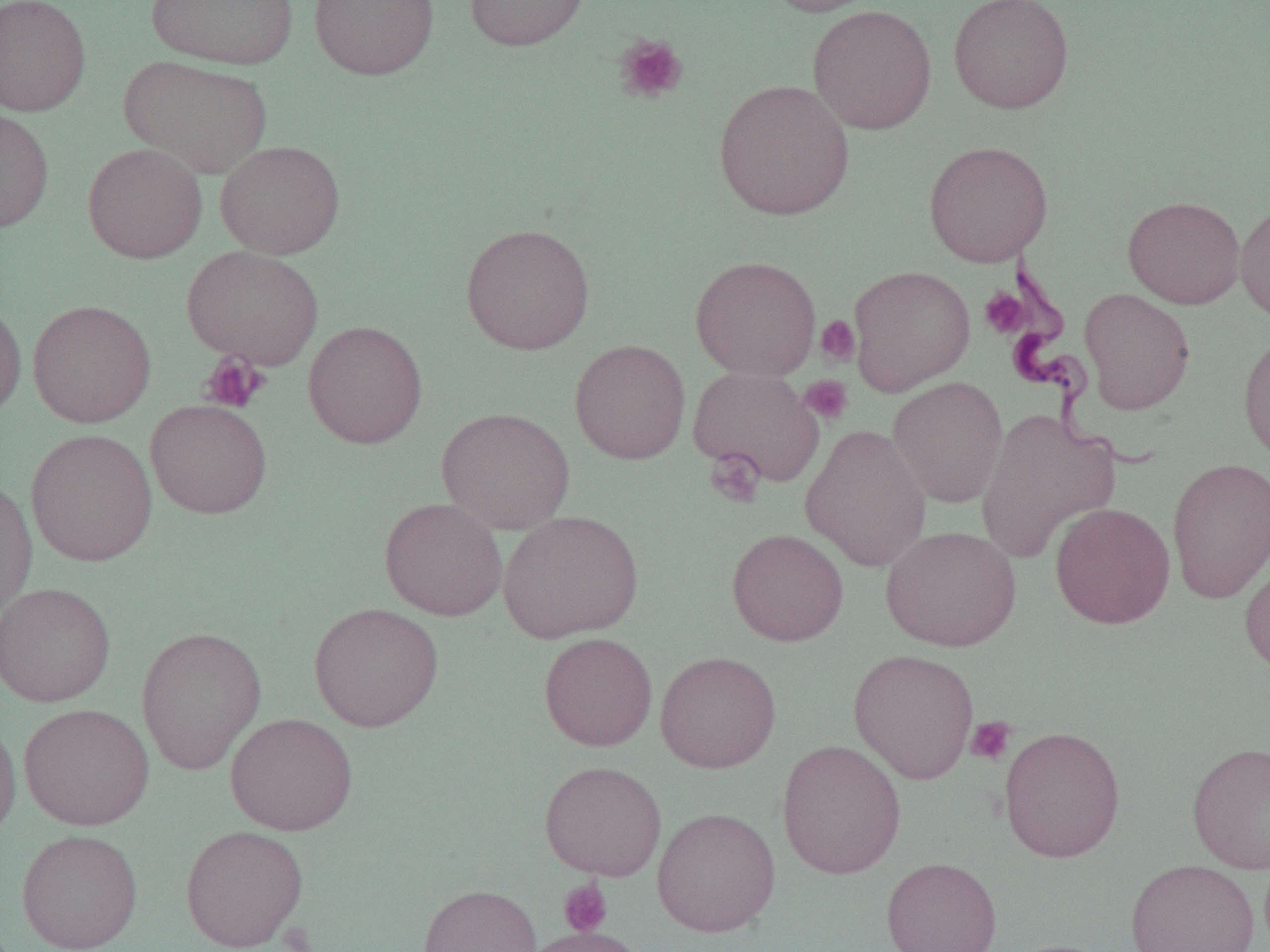
Summary:
  - Coordinate format: approximate bounding boxes as named x1/y1/x2/y2 corners in pixels
  - Uninfected red blood cell locations: (x1=0, y1=0, x2=91, y2=116), (x1=147, y1=0, x2=299, y2=69), (x1=309, y1=0, x2=439, y2=80), (x1=464, y1=0, x2=592, y2=51), (x1=762, y1=0, x2=890, y2=17), (x1=948, y1=0, x2=1074, y2=114), (x1=807, y1=5, x2=937, y2=135), (x1=119, y1=54, x2=272, y2=178), (x1=713, y1=78, x2=855, y2=221), (x1=0, y1=109, x2=54, y2=232), (x1=215, y1=140, x2=345, y2=259), (x1=923, y1=140, x2=1053, y2=267), (x1=83, y1=142, x2=207, y2=264), (x1=1123, y1=196, x2=1245, y2=309), (x1=1235, y1=200, x2=1270, y2=325), (x1=460, y1=223, x2=595, y2=355), (x1=182, y1=245, x2=323, y2=369), (x1=690, y1=256, x2=821, y2=381), (x1=848, y1=265, x2=975, y2=395), (x1=1079, y1=288, x2=1195, y2=414), (x1=0, y1=297, x2=26, y2=421), (x1=27, y1=299, x2=157, y2=428), (x1=303, y1=320, x2=427, y2=449), (x1=1238, y1=332, x2=1270, y2=465), (x1=569, y1=339, x2=691, y2=464), (x1=687, y1=366, x2=824, y2=486), (x1=888, y1=376, x2=1009, y2=508), (x1=146, y1=399, x2=272, y2=519), (x1=436, y1=407, x2=575, y2=534), (x1=974, y1=407, x2=1119, y2=564), (x1=800, y1=423, x2=932, y2=572), (x1=25, y1=428, x2=158, y2=567), (x1=1167, y1=456, x2=1270, y2=603), (x1=0, y1=477, x2=37, y2=619), (x1=379, y1=497, x2=507, y2=621), (x1=1050, y1=503, x2=1174, y2=629), (x1=498, y1=509, x2=644, y2=644), (x1=880, y1=525, x2=1021, y2=652), (x1=727, y1=528, x2=848, y2=646), (x1=1239, y1=554, x2=1270, y2=678), (x1=0, y1=582, x2=116, y2=707), (x1=308, y1=602, x2=444, y2=732), (x1=136, y1=626, x2=267, y2=775), (x1=538, y1=632, x2=658, y2=751), (x1=848, y1=649, x2=979, y2=784), (x1=655, y1=650, x2=781, y2=773), (x1=18, y1=703, x2=154, y2=830), (x1=225, y1=712, x2=358, y2=835), (x1=0, y1=716, x2=21, y2=841), (x1=998, y1=726, x2=1126, y2=863), (x1=776, y1=739, x2=907, y2=879), (x1=1187, y1=741, x2=1270, y2=874), (x1=539, y1=760, x2=666, y2=881), (x1=651, y1=806, x2=781, y2=937), (x1=180, y1=825, x2=308, y2=951), (x1=16, y1=828, x2=143, y2=952), (x1=880, y1=857, x2=1002, y2=952), (x1=1125, y1=858, x2=1260, y2=952), (x1=418, y1=884, x2=541, y2=952), (x1=520, y1=926, x2=647, y2=952), (x1=998, y1=939, x2=1119, y2=952)
  - Trypanosoma brucei locations: (x1=999, y1=253, x2=1156, y2=474)
  - Platelet locations: (x1=613, y1=34, x2=688, y2=105), (x1=979, y1=287, x2=1031, y2=339), (x1=816, y1=315, x2=861, y2=367), (x1=199, y1=352, x2=269, y2=414), (x1=799, y1=375, x2=853, y2=425), (x1=704, y1=448, x2=765, y2=507), (x1=965, y1=716, x2=1016, y2=766), (x1=558, y1=878, x2=613, y2=937)
  - Slide-level diagnosis: Trypanosoma brucei
  - Magnification: 1000x
  - Preparation: thin blood film
  - Image size: 1270×952 pixels
  - Modality: light microscopy
  - Field of view: one of a larger specimen